Assess this cell for malaria.
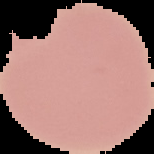

Uninfected.

Image is 154×154 pixels. From a thin blood film. Cell region segmented out of the field of view; the surrounding area is masked to black.